Name the parasite shown.
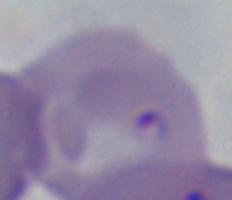
Babesia.

modality = photomicrograph
magnification = 1000x